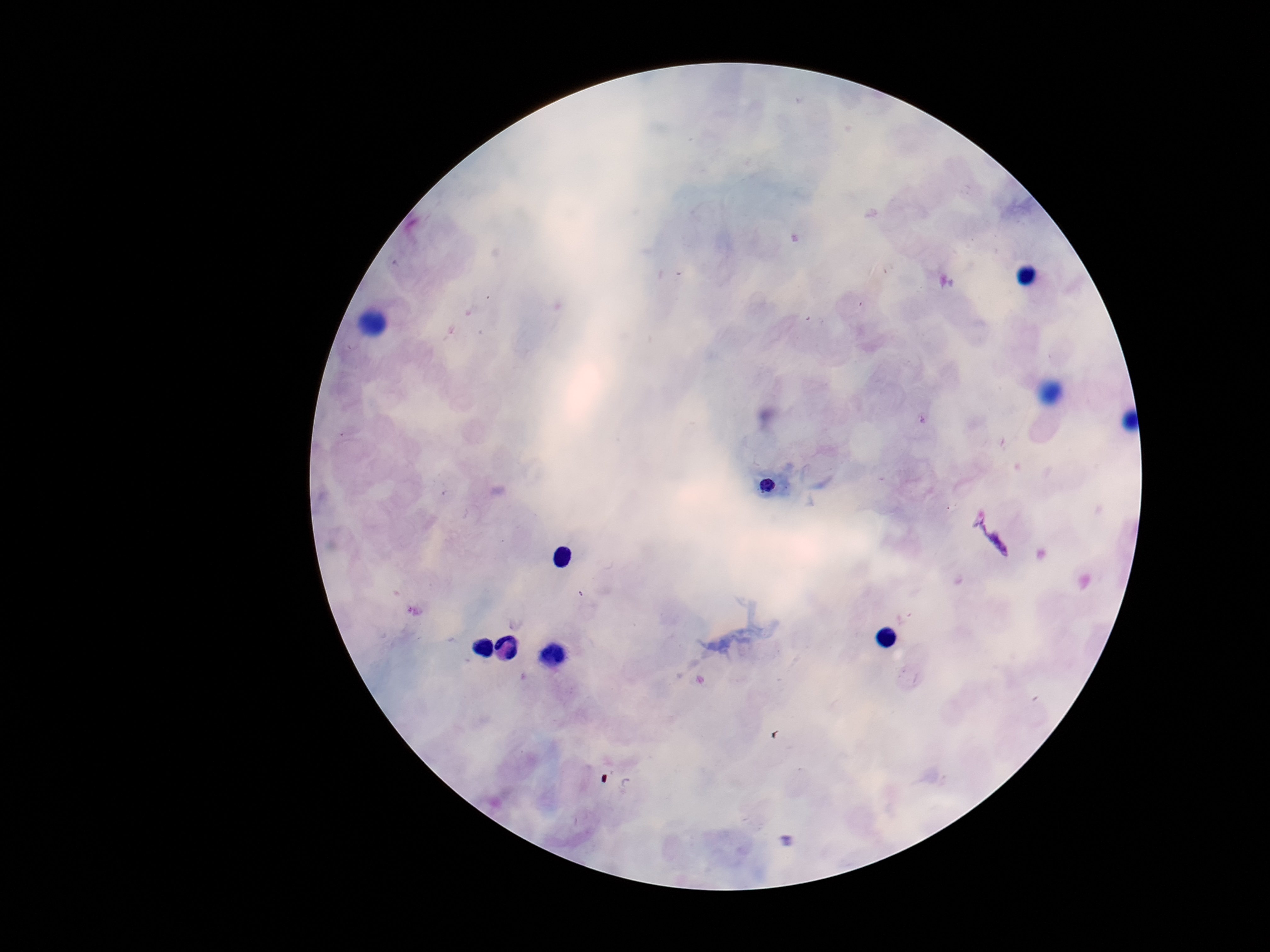

Approximate centers as [x, y] in pixels.
Summary:
  - Plasmodium parasite locations: [767, 484], [993, 541]
  - Stain: Giemsa
  - Field of view: single
  - Capture: smartphone camera through the microscope eyepiece
  - Magnification: 100x
  - Image size: 1270×952 pixels
  - Patient malaria status: infected
  - Preparation: thick peripheral-blood smear